Name the parasite shown.
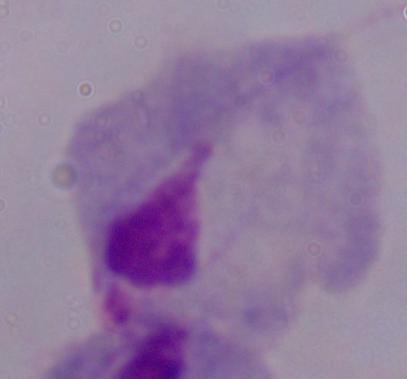
This is a trichomonad.

Photomicrograph. 1000x magnification.